Mark where platelets are.
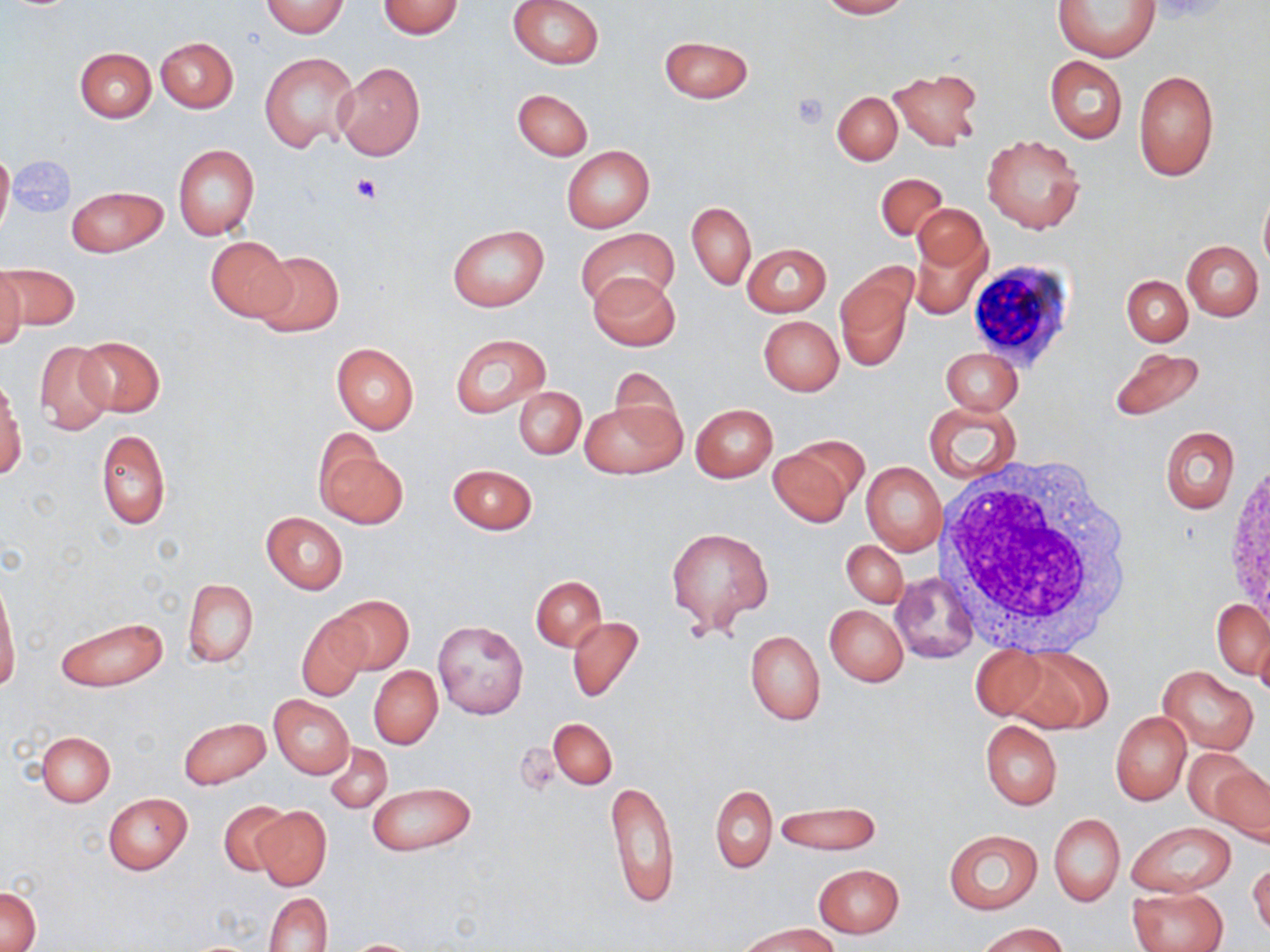

Approximate bounding boxes as named x1/y1/x2/y2 corners in pixels.
Platelets: (x1=792, y1=92, x2=830, y2=128), (x1=350, y1=171, x2=382, y2=202).

Summary:
  - White blood cell locations: (x1=969, y1=260, x2=1075, y2=377), (x1=935, y1=455, x2=1140, y2=654)
  - Uninfected red blood cell locations: (x1=377, y1=0, x2=463, y2=39), (x1=508, y1=0, x2=605, y2=69), (x1=816, y1=0, x2=910, y2=19), (x1=1053, y1=0, x2=1158, y2=63), (x1=260, y1=1, x2=349, y2=37), (x1=658, y1=35, x2=754, y2=103), (x1=155, y1=36, x2=238, y2=112), (x1=73, y1=47, x2=156, y2=122), (x1=260, y1=52, x2=358, y2=152), (x1=1045, y1=56, x2=1127, y2=143), (x1=334, y1=62, x2=425, y2=160), (x1=887, y1=67, x2=983, y2=151), (x1=1134, y1=69, x2=1218, y2=181), (x1=512, y1=88, x2=592, y2=160), (x1=833, y1=91, x2=902, y2=165), (x1=983, y1=135, x2=1085, y2=234), (x1=173, y1=144, x2=260, y2=241), (x1=0, y1=145, x2=13, y2=239), (x1=561, y1=145, x2=654, y2=232), (x1=876, y1=172, x2=947, y2=242), (x1=66, y1=186, x2=167, y2=257), (x1=1259, y1=189, x2=1270, y2=276), (x1=686, y1=201, x2=756, y2=291), (x1=912, y1=203, x2=988, y2=278), (x1=448, y1=225, x2=549, y2=311), (x1=577, y1=228, x2=679, y2=312), (x1=911, y1=235, x2=990, y2=320), (x1=205, y1=236, x2=294, y2=324), (x1=1182, y1=240, x2=1263, y2=320), (x1=742, y1=243, x2=832, y2=316), (x1=251, y1=249, x2=344, y2=338), (x1=1, y1=262, x2=79, y2=333), (x1=0, y1=265, x2=25, y2=355), (x1=835, y1=265, x2=916, y2=370), (x1=589, y1=273, x2=680, y2=352), (x1=1119, y1=274, x2=1196, y2=420), (x1=1122, y1=275, x2=1192, y2=345), (x1=758, y1=315, x2=844, y2=395), (x1=449, y1=333, x2=553, y2=419), (x1=74, y1=336, x2=166, y2=417), (x1=34, y1=340, x2=116, y2=435), (x1=330, y1=342, x2=420, y2=433), (x1=941, y1=347, x2=1022, y2=415), (x1=1108, y1=347, x2=1206, y2=422), (x1=609, y1=369, x2=684, y2=445), (x1=0, y1=377, x2=24, y2=479), (x1=513, y1=386, x2=586, y2=460), (x1=580, y1=400, x2=685, y2=480), (x1=925, y1=402, x2=1022, y2=483), (x1=690, y1=404, x2=777, y2=482), (x1=1160, y1=427, x2=1240, y2=514), (x1=97, y1=428, x2=170, y2=530), (x1=314, y1=437, x2=406, y2=529), (x1=767, y1=439, x2=863, y2=526), (x1=862, y1=462, x2=945, y2=555), (x1=448, y1=464, x2=538, y2=534), (x1=261, y1=512, x2=347, y2=593), (x1=667, y1=527, x2=773, y2=631), (x1=842, y1=540, x2=907, y2=606), (x1=891, y1=571, x2=979, y2=664), (x1=0, y1=576, x2=20, y2=695), (x1=531, y1=577, x2=606, y2=651), (x1=182, y1=579, x2=258, y2=668), (x1=330, y1=596, x2=412, y2=674), (x1=1213, y1=598, x2=1270, y2=679), (x1=824, y1=604, x2=908, y2=686), (x1=296, y1=613, x2=370, y2=701), (x1=57, y1=615, x2=167, y2=691), (x1=566, y1=616, x2=644, y2=703), (x1=432, y1=619, x2=528, y2=719), (x1=1256, y1=629, x2=1270, y2=704), (x1=745, y1=630, x2=825, y2=725), (x1=967, y1=647, x2=1049, y2=722), (x1=1004, y1=648, x2=1112, y2=732), (x1=369, y1=665, x2=442, y2=748), (x1=1158, y1=665, x2=1259, y2=755), (x1=269, y1=694, x2=354, y2=779), (x1=1110, y1=711, x2=1191, y2=805), (x1=178, y1=717, x2=270, y2=789), (x1=547, y1=718, x2=617, y2=790), (x1=981, y1=720, x2=1062, y2=810), (x1=36, y1=730, x2=115, y2=806), (x1=326, y1=743, x2=392, y2=813), (x1=1184, y1=746, x2=1262, y2=828), (x1=1209, y1=765, x2=1269, y2=845), (x1=606, y1=781, x2=679, y2=909), (x1=367, y1=782, x2=476, y2=855), (x1=709, y1=785, x2=776, y2=873), (x1=102, y1=792, x2=192, y2=874), (x1=218, y1=800, x2=292, y2=877), (x1=773, y1=800, x2=882, y2=855), (x1=252, y1=805, x2=331, y2=890), (x1=1049, y1=814, x2=1124, y2=906), (x1=1126, y1=821, x2=1236, y2=898), (x1=943, y1=829, x2=1043, y2=913), (x1=1249, y1=858, x2=1270, y2=937), (x1=814, y1=864, x2=903, y2=938), (x1=2, y1=886, x2=41, y2=950), (x1=1129, y1=887, x2=1228, y2=952), (x1=264, y1=892, x2=333, y2=952), (x1=973, y1=921, x2=1067, y2=952), (x1=742, y1=923, x2=836, y2=952), (x1=340, y1=939, x2=426, y2=951)
  - Slide-level diagnosis: no evidence of blood parasites
  - Magnification: 1000x
  - Stain: May-Grünwald-Giemsa
  - Field of view: single
  - Preparation: thin blood film
  - Modality: optical microscopy
  - Image size: 1270×952 pixels